Classify this cell by malaria status.
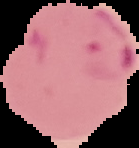

It is parasitized.

Image is 139×148 pixels. Segmented cell region on a black background. From a thin blood smear.